Name the parasite shown.
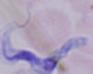
A trypanosome.

Photomicrograph. 1000x magnification.